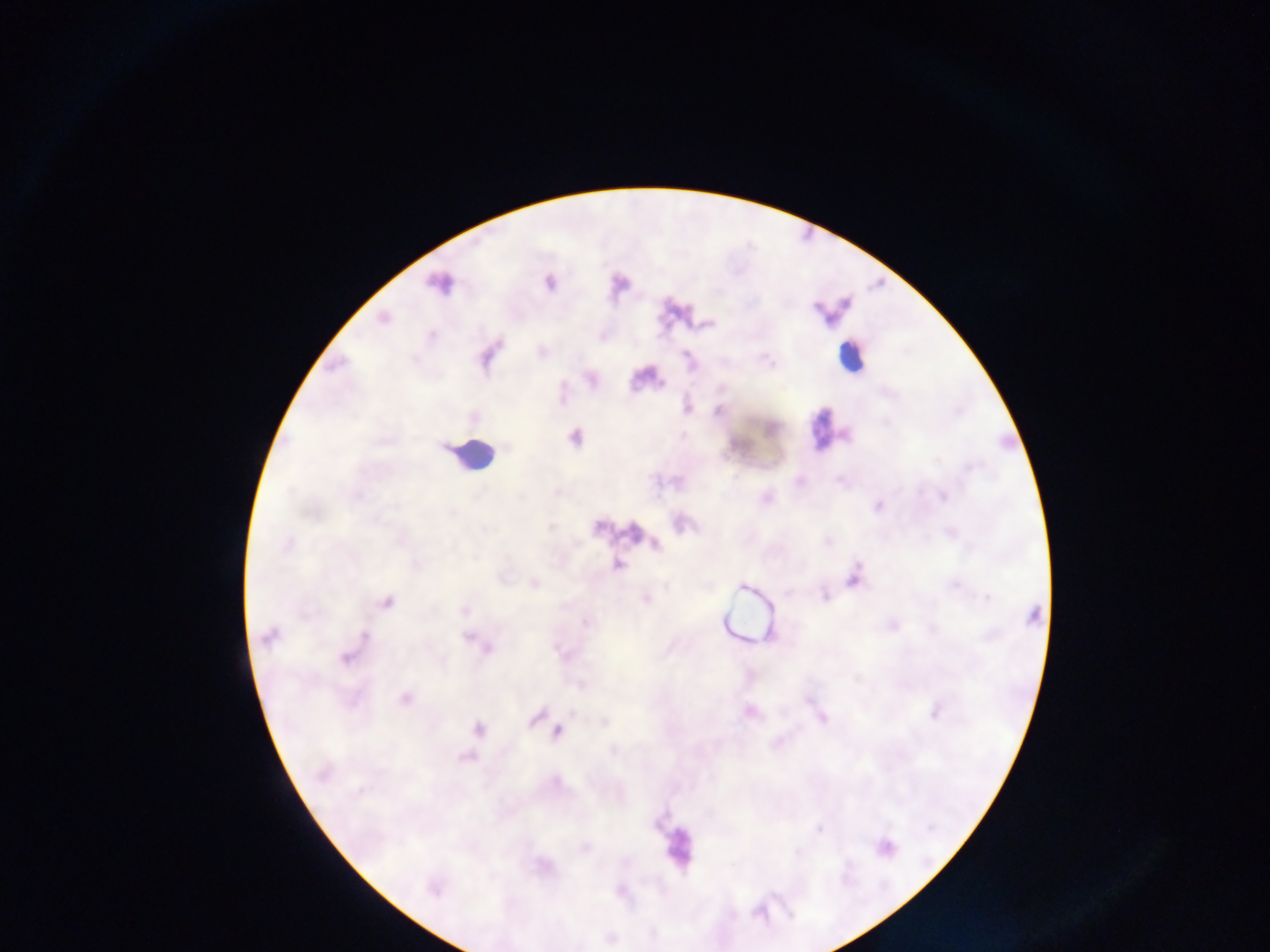
Approximate centers as [x, y] in pixels.
Summary:
  - Leukocyte locations: [851, 357], [825, 428], [474, 455], [674, 847]
  - Plasmodium parasite locations: [439, 283], [550, 283], [817, 309], [383, 319], [432, 335], [591, 379], [687, 408], [718, 411], [772, 428], [574, 438], [970, 467], [942, 496], [766, 498], [878, 506], [950, 534], [827, 541], [287, 544], [656, 544], [618, 565], [853, 578], [535, 584], [956, 586], [741, 587], [824, 596], [988, 598], [646, 599], [387, 602], [464, 611], [1033, 615], [892, 626], [268, 636], [364, 636], [467, 637], [488, 648], [345, 658], [580, 684], [405, 699], [809, 700], [935, 711], [750, 712], [535, 718], [822, 718], [605, 722], [479, 729], [558, 732], [613, 750], [322, 773], [888, 847], [433, 889]
  - Preparation: thick blood film
  - Image size: 1270×952 pixels
  - Capture: mobile-phone photograph through a microscope
  - Field of view: single
  - Country: Ghana